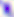

magnification = 400x
identification = Toxoplasma gondii
modality = micrograph